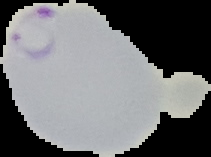

image size = 211×157 pixels
image type = segmented cell region on a black background
preparation = thin blood smear
malaria status = parasitized